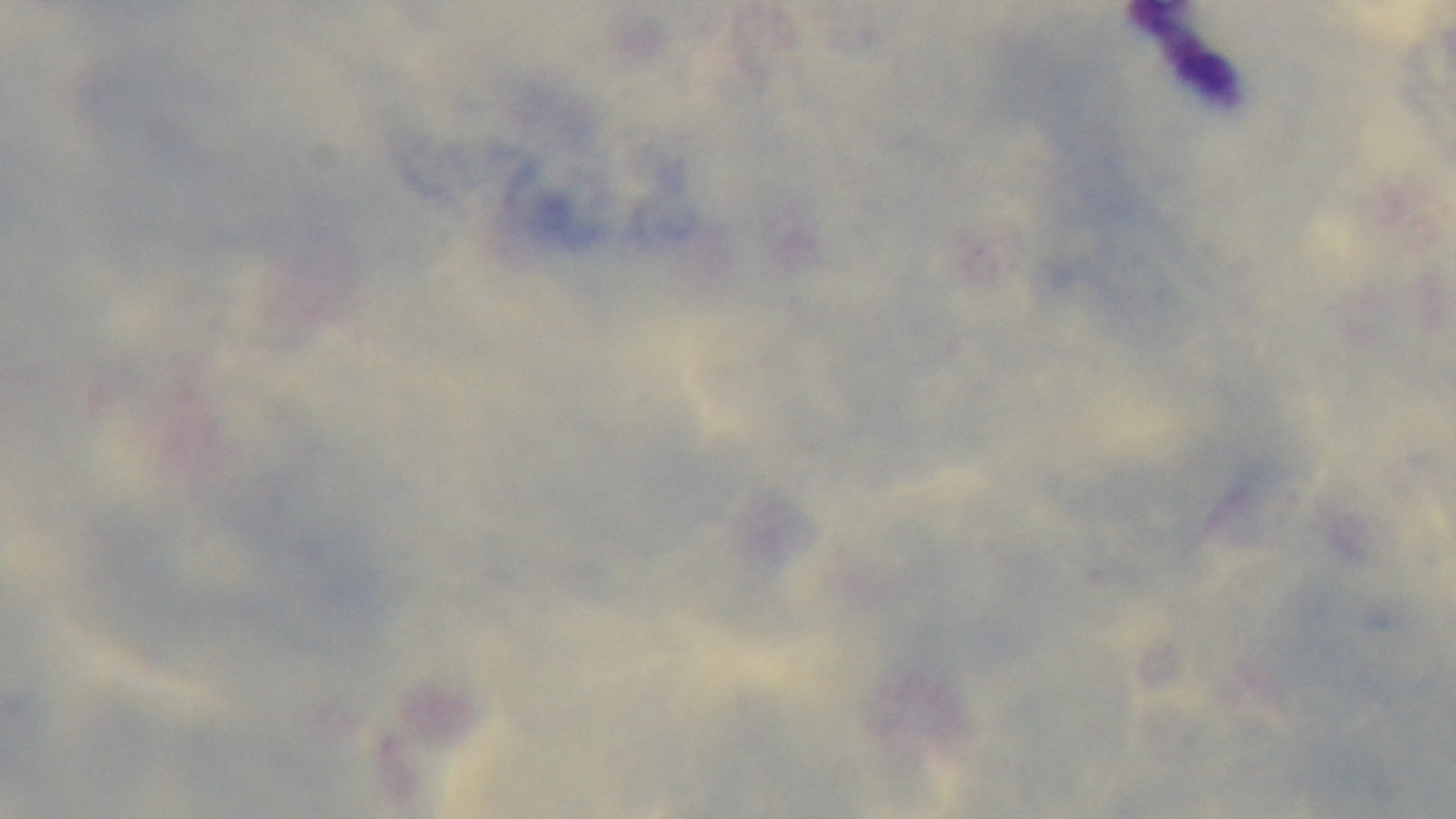

stain = Giemsa
modality = light microscopy
objective = 100x oil immersion
malaria status = uninfected
field of view = one from the slide
capture = mounted 4K digital camera
preparation = thick blood film